Describe the morphology of the red blood cells.
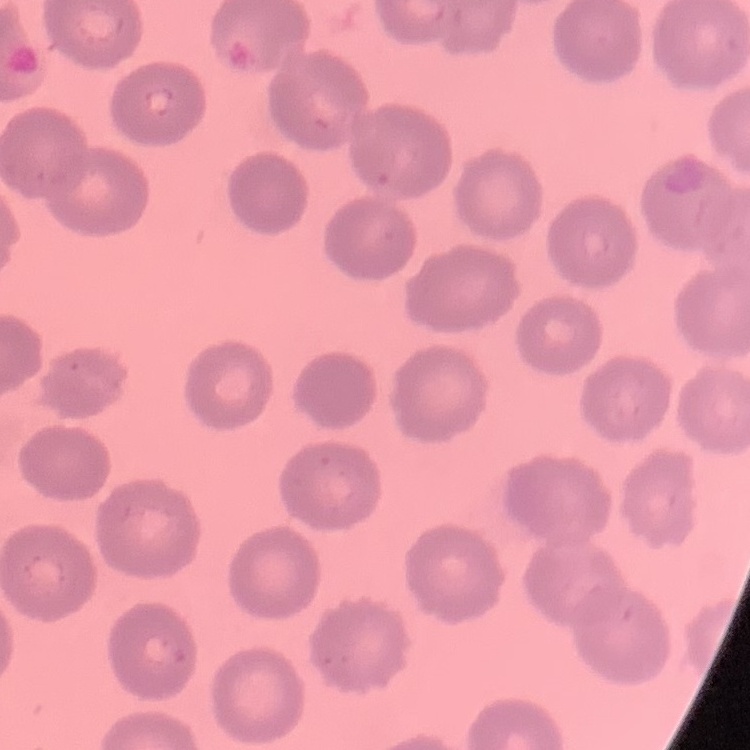

No rouleaux formation.

Summary:
  - Image type: square crop of a larger photomicrograph
  - Preparation: thin blood film
  - Stain: Field's or Giemsa